Give the position of every leukocyte visible.
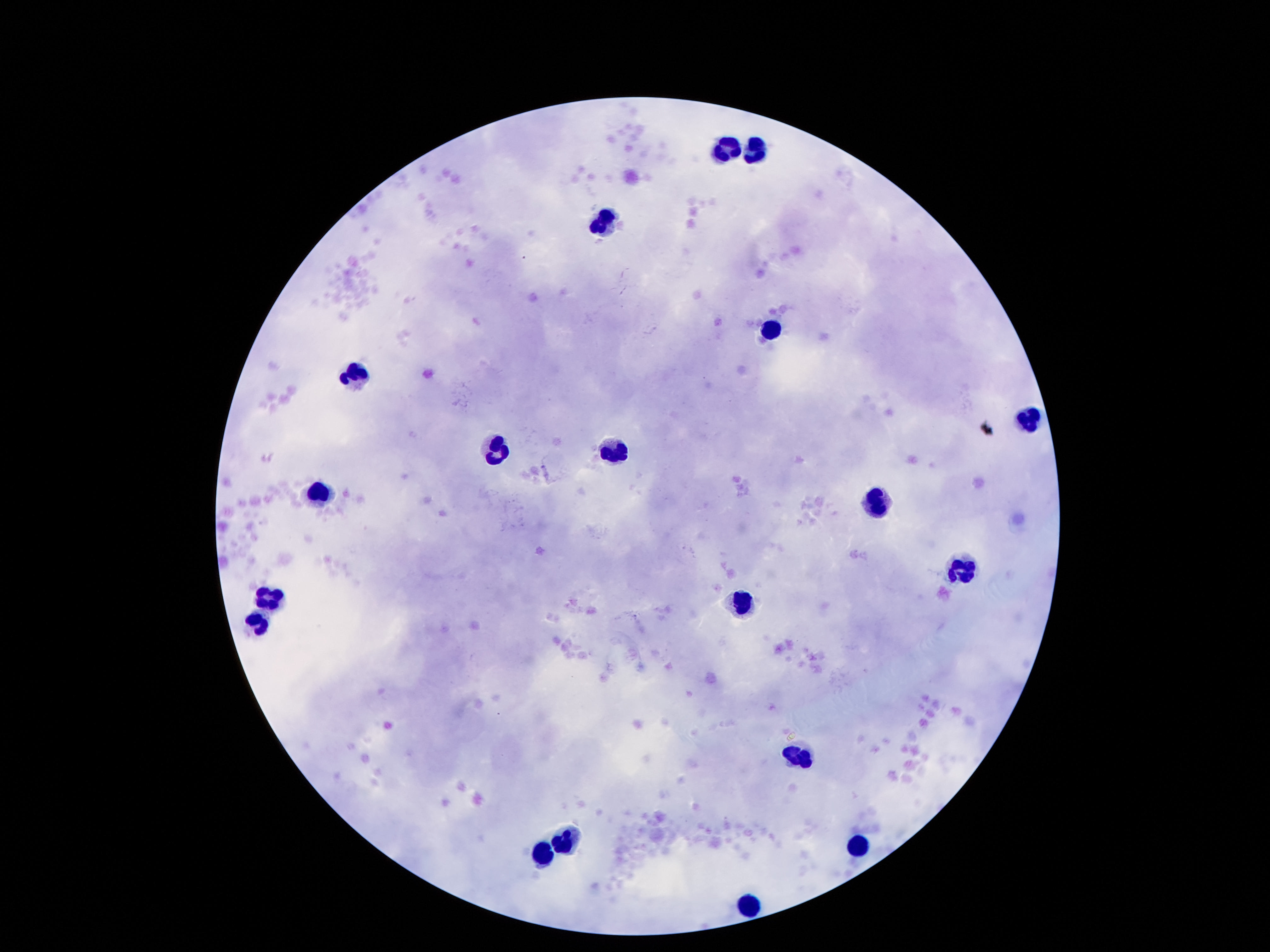

Approximate centers as (x, y) in pixels.
Leukocytes: (759, 147), (725, 151), (608, 218), (768, 330), (356, 371), (1029, 419), (494, 449), (615, 449), (320, 490), (876, 503), (958, 569), (268, 597), (742, 604), (257, 623), (786, 642), (798, 755), (565, 836), (858, 843), (539, 854), (755, 901).

patient_malaria_status: uninfected
image_size: 1270×952 pixels
magnification: 100x
preparation: thick blood smear
capture: smartphone camera through the microscope eyepiece
field_of_view: single
stain: Giemsa